Locate every blood parasite and identify its species.
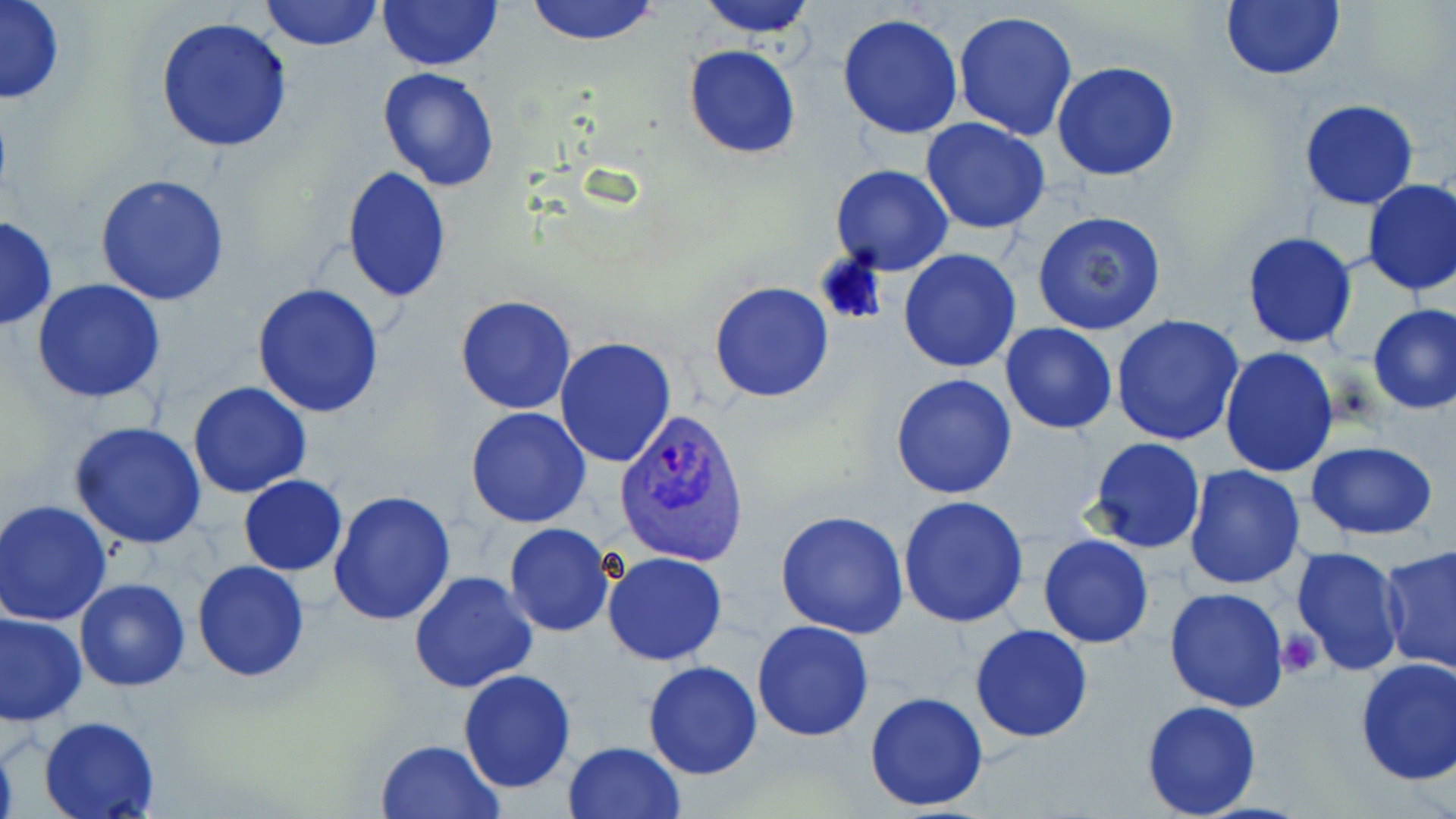

Approximate bounding boxes as (x1, y1, x2, y2) in pixels.
Plasmodium vivax-infected red blood cells: (613, 406, 753, 567).
No Plasmodium falciparum, Plasmodium ovale, Plasmodium malariae, Babesia divergens, or Trypanosoma brucei observed.

Platelet locations: (1278, 629, 1324, 678). Uninfected red blood cell locations: (0, 0, 64, 105), (260, 0, 382, 51), (378, 0, 502, 71), (521, 0, 664, 46), (693, 0, 820, 40), (1221, 0, 1346, 80), (952, 10, 1079, 142), (838, 12, 962, 140), (152, 17, 295, 155), (682, 45, 803, 160), (1051, 61, 1179, 182), (377, 66, 501, 190), (1299, 99, 1418, 209), (921, 119, 1051, 235), (831, 165, 954, 276), (340, 167, 451, 302), (95, 172, 230, 305), (1361, 177, 1456, 296), (1033, 210, 1168, 336), (0, 214, 56, 331), (1241, 231, 1357, 351), (898, 248, 1021, 373), (32, 279, 165, 404), (709, 281, 835, 403), (252, 283, 384, 417), (455, 295, 577, 415), (1368, 305, 1456, 415), (1112, 315, 1245, 447), (1000, 323, 1119, 435), (553, 336, 675, 469), (1219, 347, 1339, 478), (890, 374, 1017, 498), (187, 381, 311, 498), (466, 407, 592, 529), (67, 422, 208, 550), (1087, 437, 1206, 554), (1305, 440, 1439, 541), (1184, 465, 1306, 590), (239, 475, 347, 574), (328, 491, 457, 627), (897, 494, 1030, 629), (2, 499, 114, 625), (775, 511, 909, 640), (504, 524, 615, 637), (1038, 534, 1154, 649), (1379, 544, 1456, 673), (1291, 546, 1408, 675), (603, 552, 728, 666), (192, 560, 309, 682), (409, 570, 539, 694), (75, 577, 190, 691), (1163, 588, 1291, 713), (0, 603, 181, 717), (1, 612, 87, 726), (752, 621, 874, 740), (970, 624, 1094, 743), (1353, 656, 1456, 786), (642, 660, 763, 780), (459, 669, 576, 793), (864, 690, 990, 812), (1140, 700, 1263, 819), (38, 715, 161, 819), (0, 734, 18, 816), (375, 738, 506, 819), (562, 740, 687, 819). Slide-level diagnosis: Plasmodium vivax. Light microscopy. Image is 1456×819 pixels. May-Grünwald-Giemsa-stained preparation. Thin blood smear. Captured at 1000x magnification. One field of a larger specimen.